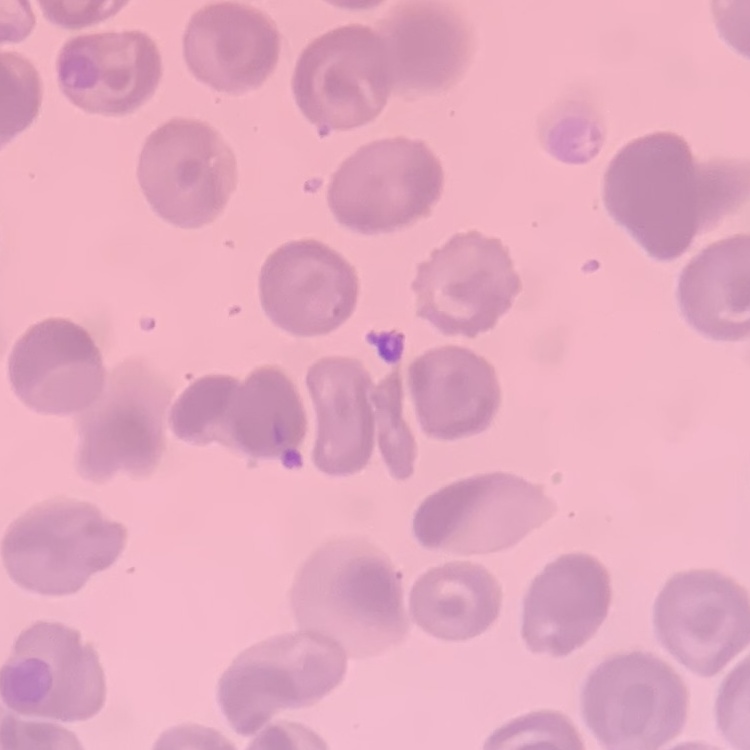
Summary:
  - Erythrocyte morphology: no rouleaux formation
  - Image type: one tile cut from a larger photomicrograph
  - Stain: Field's or Giemsa
  - Preparation: thin peripheral smear